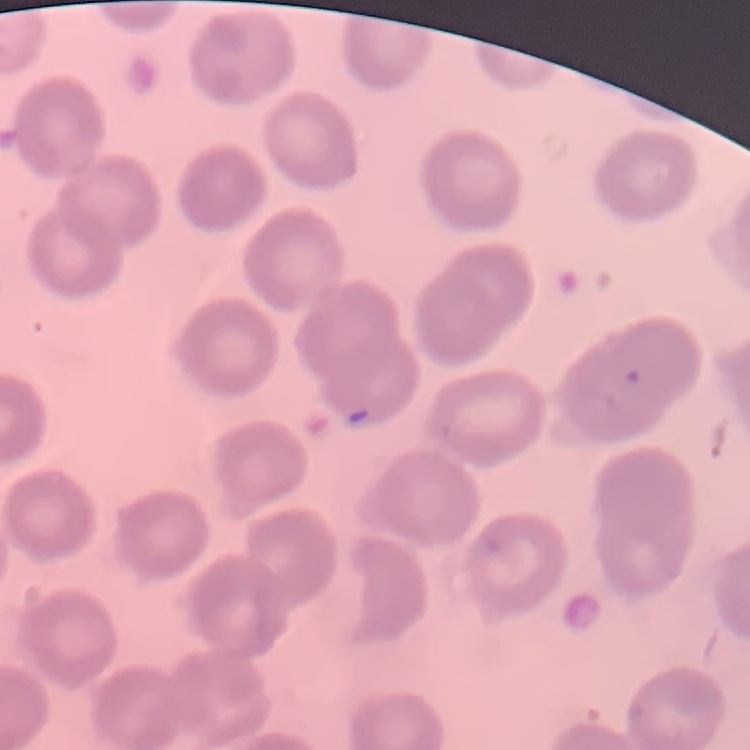
The red blood cells show no rouleaux formation. Field's or Giemsa stain. Thin blood smear. Square crop of a larger photomicrograph.